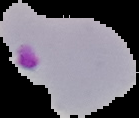 From a thin blood film. Segmented cell region on a black background. Malaria status: parasitized. Image is 139×118 pixels.